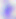
400x magnification. Toxoplasma gondii is shown. Photomicrograph.